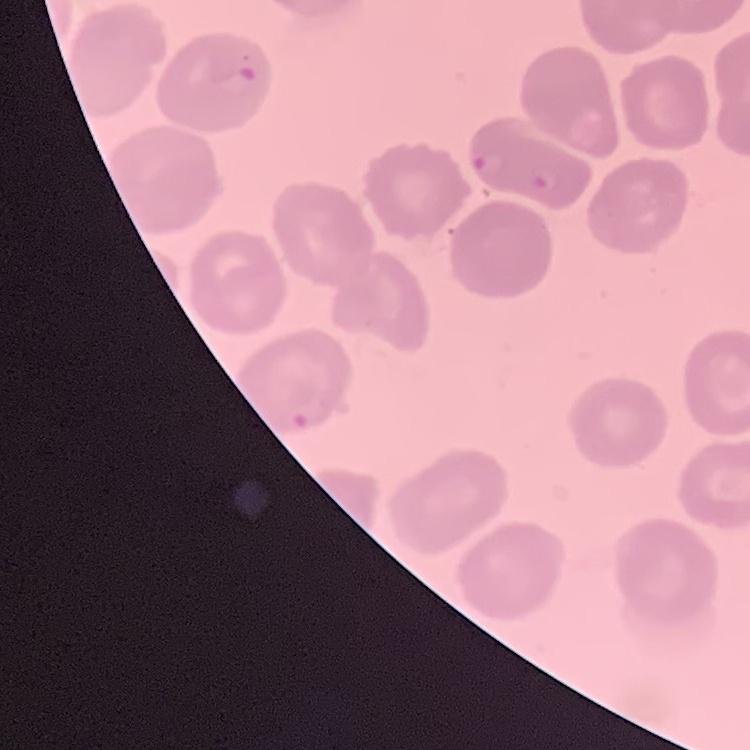 The erythrocytes exhibit no rouleaux formation. Thin blood smear. Square crop of a larger photomicrograph. Stained with either Field's or Giemsa.